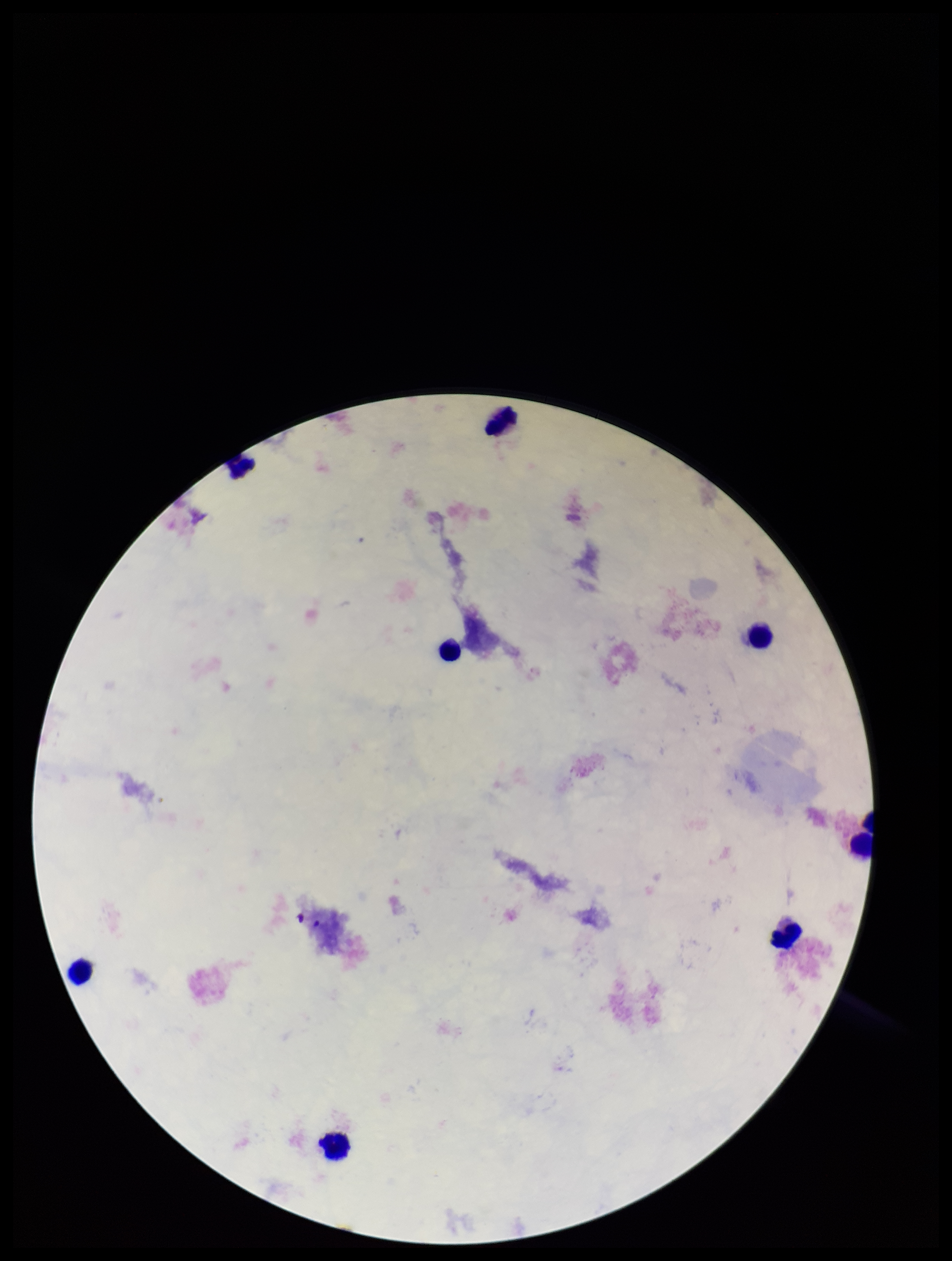

Summary:
  - Capture: smartphone photograph through the microscope eyepiece
  - Plasmodium parasites: none identified
  - Parasite count: 0
  - Field of view: single
  - Patient malaria status: negative
  - Image size: 952×1261 pixels
  - Preparation: thick smear
  - Leukocyte count: 8
  - Stain: Giemsa